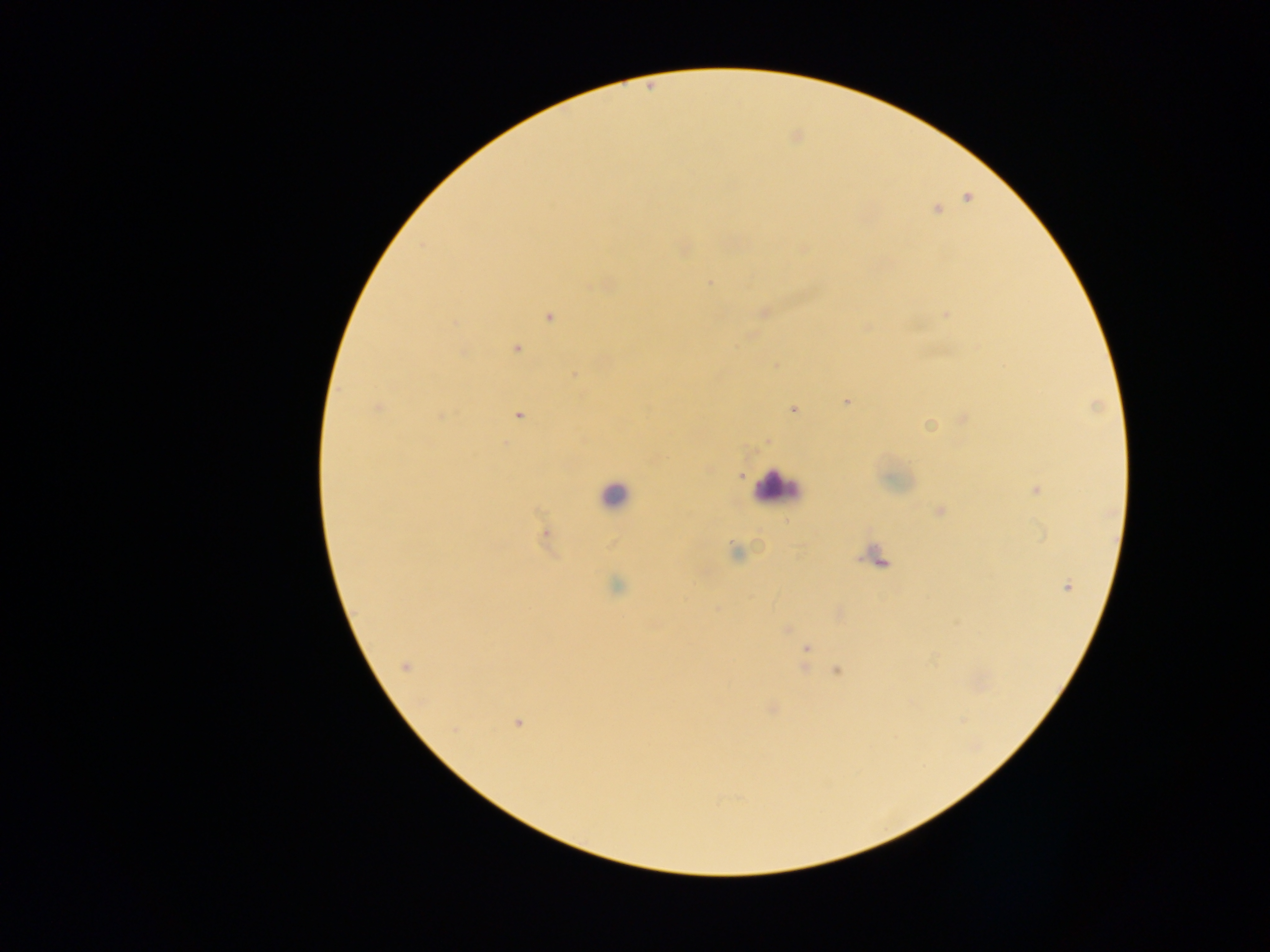
preparation = thick blood smear
malaria parasite locations = approximate centers as {x, y} in pixels: {966, 197}, {937, 209}, {802, 248}, {683, 249}, {709, 282}, {605, 283}, {763, 312}, {946, 313}, {550, 317}, {866, 327}, {515, 348}, {775, 366}, {574, 375}, {847, 401}, {376, 408}, {793, 408}, {518, 414}, {439, 416}, {964, 419}, {929, 424}, {767, 441}, {741, 474}, {1036, 488}, {939, 511}, {545, 534}, {736, 552}, {616, 586}, {1067, 587}, {786, 628}, {806, 648}, {405, 666}, {837, 670}, {772, 708}, {518, 722}
country = Ghana
capture = mobile-phone photograph through a microscope
leukocyte locations = approximate centers as {x, y} in pixels: {777, 488}, {614, 495}, {878, 557}
image size = 1270×952 pixels
field of view = single